Outline each uninfected red blood cell.
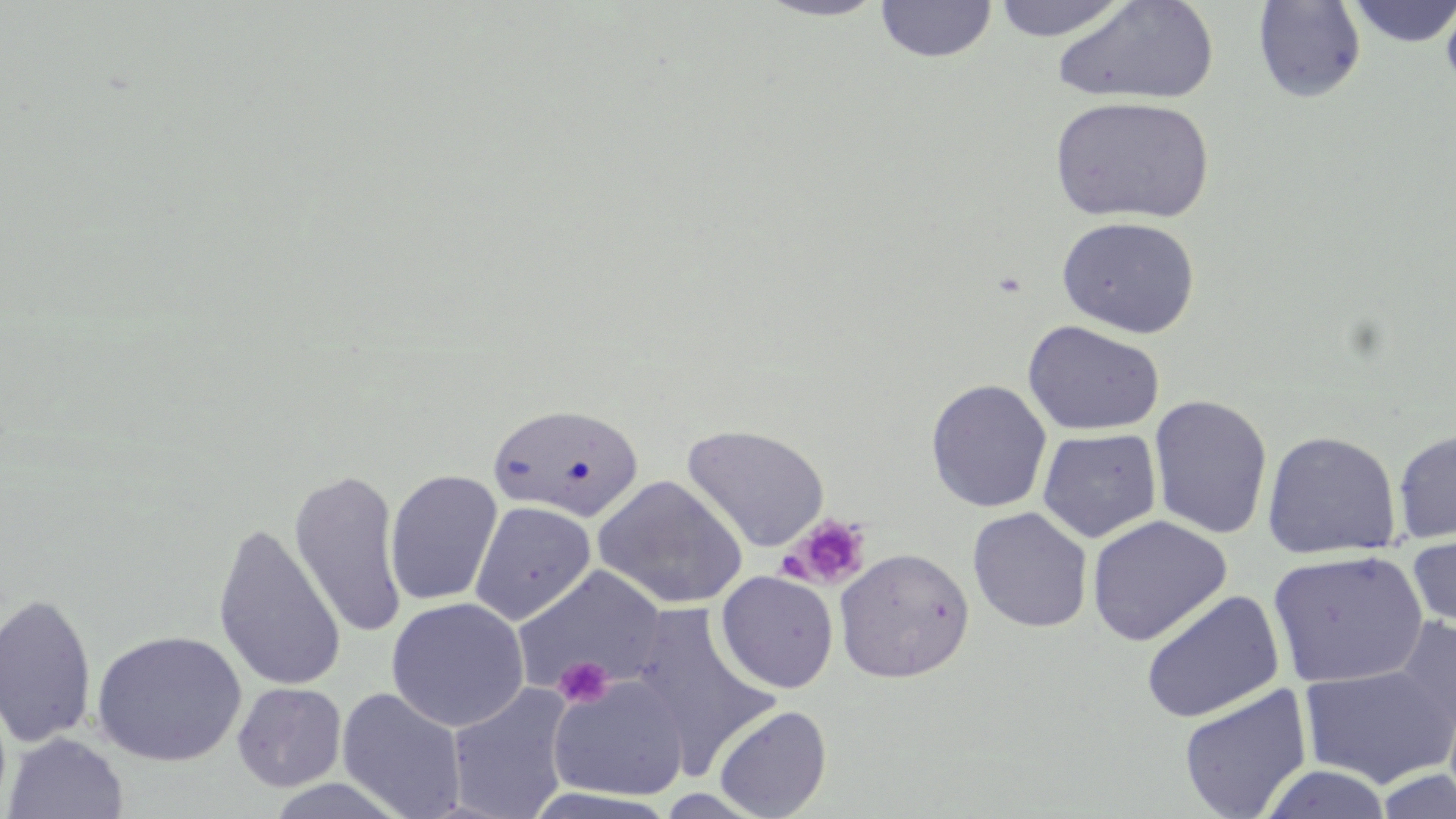
Approximate bounding boxes as (x1,y1)-(x2,y2) corner pairs in pixels.
Uninfected red blood cells: (755,0)-(890,22), (875,0)-(997,63), (990,0)-(1133,41), (1345,0)-(1456,47), (1440,0)-(1456,101), (1054,1)-(1220,107), (1252,1)-(1367,103), (1050,94)-(1215,225), (1056,215)-(1201,338), (1022,320)-(1165,436), (926,379)-(1052,513), (1149,394)-(1273,540), (488,402)-(644,522), (681,423)-(830,553), (1037,428)-(1162,543), (1393,428)-(1456,545), (1261,430)-(1401,560), (289,468)-(407,639), (384,469)-(503,607), (593,474)-(748,610), (469,500)-(596,625), (968,507)-(1093,633), (1087,515)-(1232,646), (212,522)-(346,693), (1408,527)-(1456,632), (834,547)-(974,683), (1266,548)-(1429,689), (511,566)-(666,697), (716,570)-(839,694), (1140,590)-(1284,724), (0,592)-(97,749), (386,596)-(530,732), (630,604)-(779,774), (1388,617)-(1456,743), (91,630)-(247,766), (1298,664)-(1456,789), (547,675)-(689,803), (232,681)-(347,792), (446,683)-(575,819), (1179,685)-(1313,819), (336,688)-(468,818), (713,704)-(832,819), (3,732)-(129,818), (1260,765)-(1393,819), (1375,768)-(1456,819).

Platelet locations: (789,514)-(871,588), (551,654)-(613,709). Slide-level diagnosis: negative for blood parasites. One field of a larger specimen. Light microscopy. 1000x magnification. Image is 1456×819 pixels. May-Grünwald-Giemsa-stained preparation. Thin blood smear.